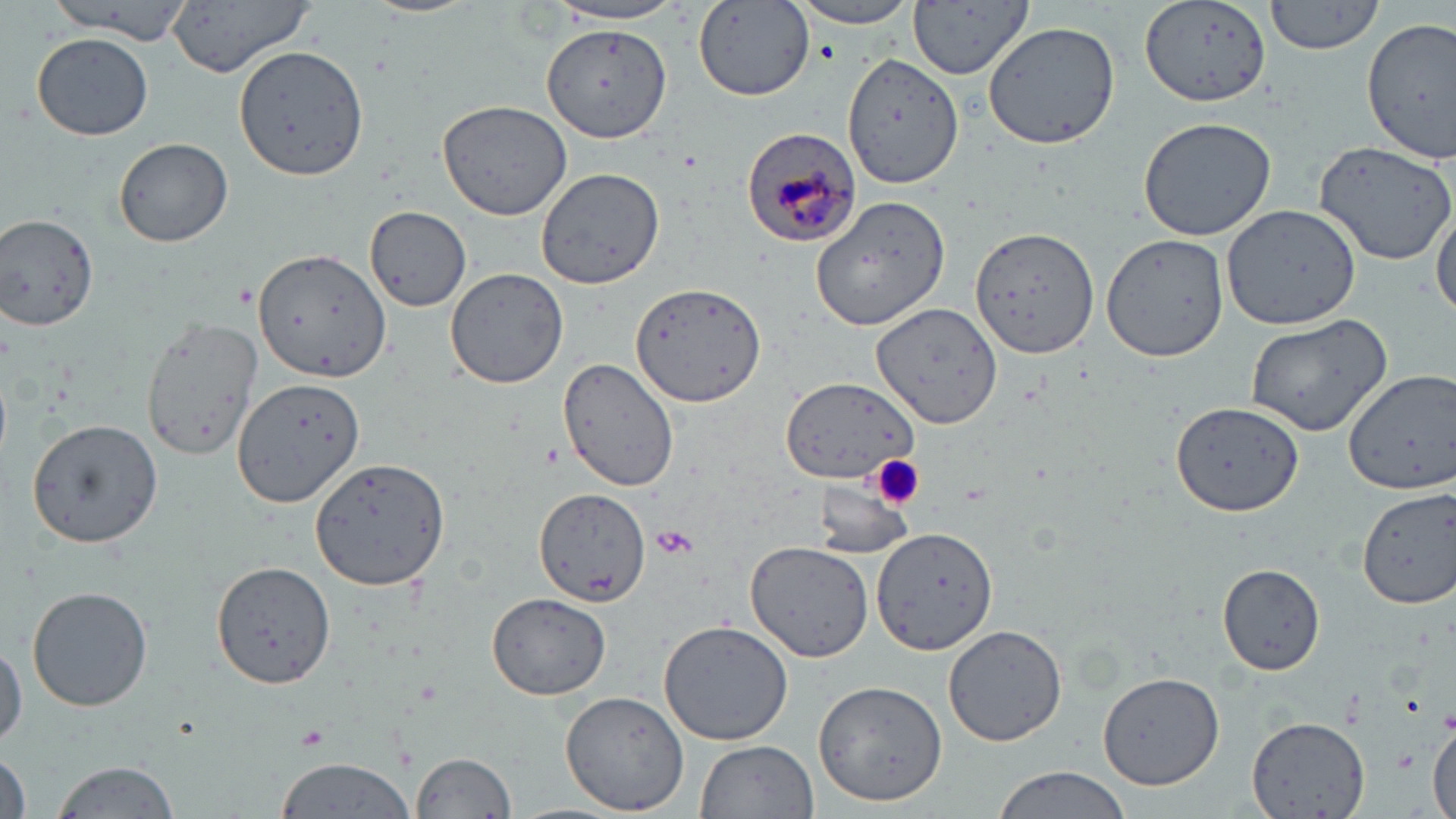 Approximate bounding boxes as [x1, y1, x2, y2] in pixels. Plasmodium malariae-infected red blood cell locations: [740, 124, 862, 249]. Platelet locations: [872, 455, 926, 509], [651, 525, 699, 559], [294, 725, 329, 753]. Uninfected red blood cell locations: [47, 0, 195, 39], [165, 0, 318, 76], [366, 0, 479, 19], [908, 0, 1034, 81], [1142, 0, 1274, 108], [1263, 0, 1387, 55], [784, 1, 926, 30], [695, 2, 815, 101], [546, 3, 690, 27], [1361, 17, 1456, 161], [982, 20, 1120, 151], [542, 24, 672, 143], [33, 32, 152, 140], [234, 43, 370, 180], [843, 53, 962, 188], [435, 98, 573, 221], [1138, 115, 1278, 243], [114, 138, 234, 247], [1314, 139, 1456, 264], [537, 168, 665, 290], [813, 193, 952, 331], [1431, 197, 1456, 322], [364, 205, 473, 312], [1222, 205, 1362, 329], [1, 215, 99, 331], [971, 224, 1099, 356], [1099, 232, 1229, 363], [254, 247, 391, 383], [443, 266, 568, 390], [630, 280, 766, 407], [873, 302, 1003, 427], [1243, 312, 1392, 439], [142, 315, 264, 461], [558, 356, 681, 492], [1341, 367, 1456, 497], [781, 376, 918, 486], [233, 377, 365, 507], [1170, 398, 1303, 517], [26, 418, 163, 547], [311, 457, 451, 592], [810, 480, 915, 558], [534, 487, 650, 607], [1356, 487, 1456, 608], [871, 527, 998, 654], [744, 539, 876, 663], [213, 559, 338, 689], [1218, 564, 1326, 675], [27, 585, 153, 713], [487, 593, 610, 699], [658, 619, 794, 746], [944, 624, 1068, 747], [1, 638, 25, 752], [1095, 670, 1223, 791], [810, 677, 948, 809], [559, 687, 694, 815], [1429, 715, 1456, 819], [1246, 716, 1369, 819], [697, 739, 818, 819], [1, 750, 32, 819], [409, 751, 517, 819], [272, 756, 416, 819], [50, 759, 183, 819], [990, 766, 1137, 819]. Slide-level diagnosis: Plasmodium malariae. May-Grünwald-Giemsa-stained preparation. Light microscopy. One field of a larger specimen. 1000x magnification. Image is 1456×819 pixels. Thin blood film.